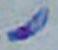
Summary:
  - Modality: photomicrograph
  - Magnification: 1000x
  - Identification: Toxoplasma gondii